State the blood parasite species.
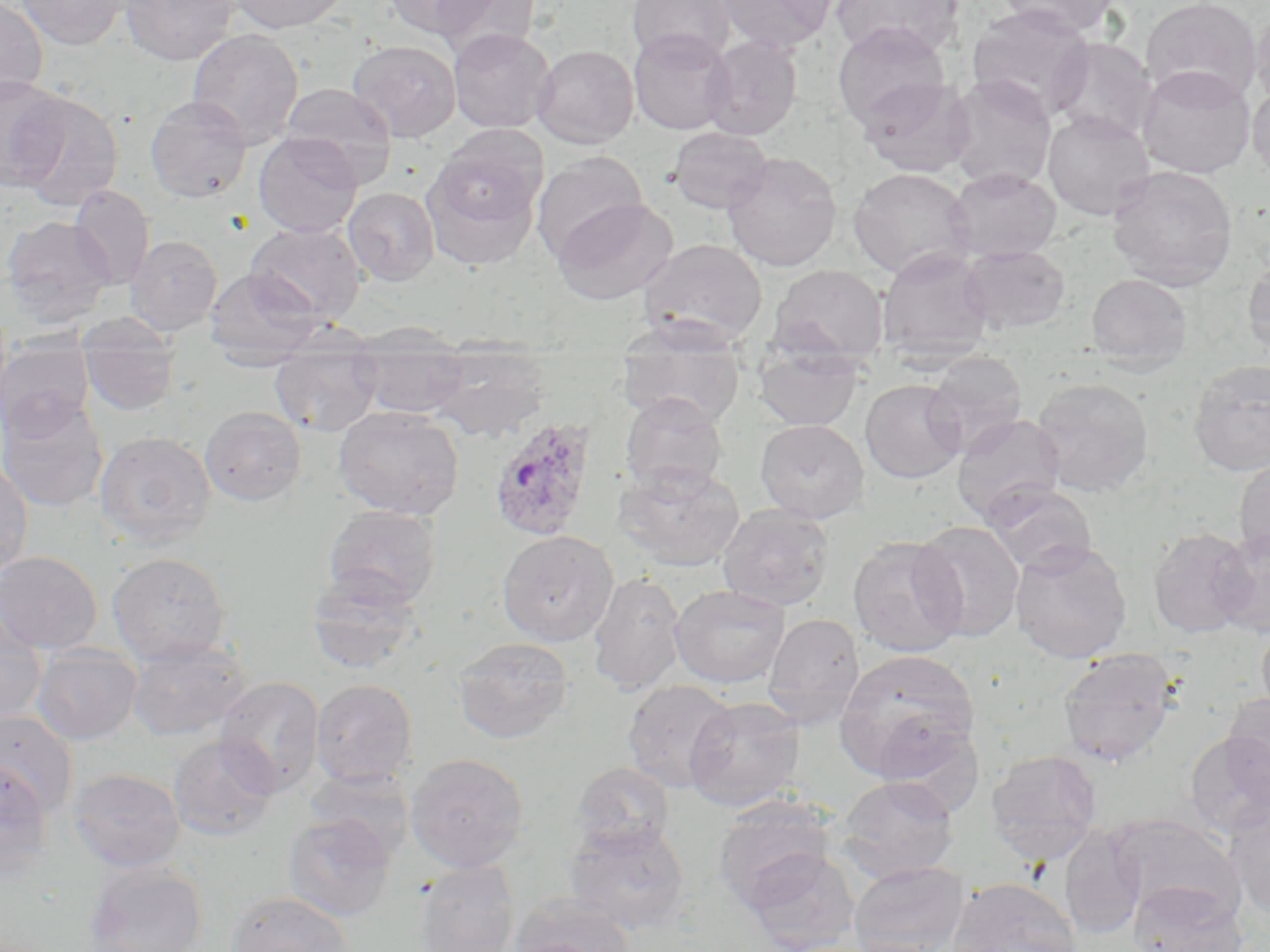
Plasmodium ovale.

Approximate bounding boxes as [x1, y1, x2, y2] in pixels. Uninfected red blood cell locations: [0, 0, 48, 104], [15, 0, 130, 50], [120, 0, 240, 65], [227, 0, 351, 33], [383, 0, 499, 40], [429, 0, 542, 58], [627, 0, 735, 65], [715, 0, 837, 53], [830, 0, 964, 61], [995, 0, 1119, 36], [1141, 0, 1262, 105], [966, 4, 1095, 119], [1251, 5, 1270, 109], [832, 24, 952, 131], [628, 27, 735, 135], [187, 28, 304, 150], [448, 28, 555, 133], [701, 34, 802, 141], [1048, 37, 1158, 144], [348, 40, 461, 142], [532, 44, 638, 148], [1137, 66, 1256, 179], [0, 75, 69, 191], [945, 76, 1057, 191], [858, 77, 975, 178], [279, 82, 397, 176], [1248, 82, 1270, 183], [13, 90, 123, 212], [145, 95, 252, 203], [1042, 110, 1155, 220], [668, 126, 773, 214], [252, 133, 363, 238], [421, 146, 544, 270], [722, 151, 842, 272], [531, 153, 649, 261], [1106, 165, 1238, 291], [848, 167, 975, 280], [946, 167, 1061, 261], [69, 186, 155, 290], [343, 187, 440, 287], [552, 196, 678, 304], [0, 216, 116, 326], [245, 222, 366, 325], [125, 234, 222, 336], [638, 238, 768, 347], [959, 245, 1071, 336], [876, 248, 995, 364], [1242, 254, 1270, 359], [769, 264, 888, 365], [204, 266, 322, 369], [1085, 273, 1193, 371], [77, 315, 181, 416], [616, 326, 746, 429], [353, 332, 472, 421], [0, 337, 94, 438], [270, 343, 383, 436], [424, 343, 552, 443], [753, 346, 864, 432], [923, 351, 1028, 454], [1188, 360, 1270, 477], [1031, 377, 1155, 498], [860, 379, 966, 484], [0, 392, 109, 513], [619, 393, 730, 497], [200, 406, 306, 506], [333, 406, 464, 520], [951, 414, 1066, 526], [755, 419, 869, 523], [95, 431, 216, 547], [1234, 455, 1270, 563], [0, 461, 34, 578], [613, 462, 745, 573], [982, 484, 1097, 576], [717, 504, 835, 611], [323, 505, 441, 609], [911, 520, 1025, 642], [1147, 528, 1255, 639], [1210, 528, 1269, 637], [497, 530, 618, 646], [847, 536, 967, 658], [1009, 539, 1132, 663], [0, 550, 102, 654], [108, 552, 232, 665], [306, 568, 424, 674], [587, 573, 687, 695], [669, 585, 791, 689], [0, 609, 47, 727], [763, 613, 865, 728], [1256, 619, 1270, 725], [453, 636, 573, 743], [126, 638, 251, 740], [31, 643, 142, 745], [835, 649, 980, 780], [1057, 649, 1179, 767], [215, 676, 325, 797], [310, 678, 418, 787], [621, 679, 738, 793], [1221, 693, 1270, 804], [684, 695, 806, 812], [0, 710, 79, 820], [871, 716, 984, 809], [1183, 731, 1270, 838], [168, 735, 278, 841], [985, 749, 1103, 864], [405, 753, 530, 872], [0, 761, 54, 881], [572, 761, 676, 855], [69, 768, 186, 872], [304, 769, 415, 862], [834, 775, 959, 883], [712, 796, 836, 911], [1226, 799, 1270, 920], [283, 814, 396, 922], [1109, 815, 1243, 922], [564, 820, 691, 932], [1060, 828, 1146, 939], [743, 848, 861, 952], [84, 860, 207, 952], [414, 860, 519, 951], [848, 860, 970, 952], [946, 877, 1082, 952], [1129, 881, 1247, 952], [226, 891, 354, 952], [513, 892, 635, 952], [503, 937, 620, 952]. Plasmodium ovale-infected red blood cell locations: [487, 418, 598, 542]. Image is 1270×952 pixels. Light microscopy. May-Grünwald-Giemsa stain. Single field of view. 1000x magnification. Thin blood film.